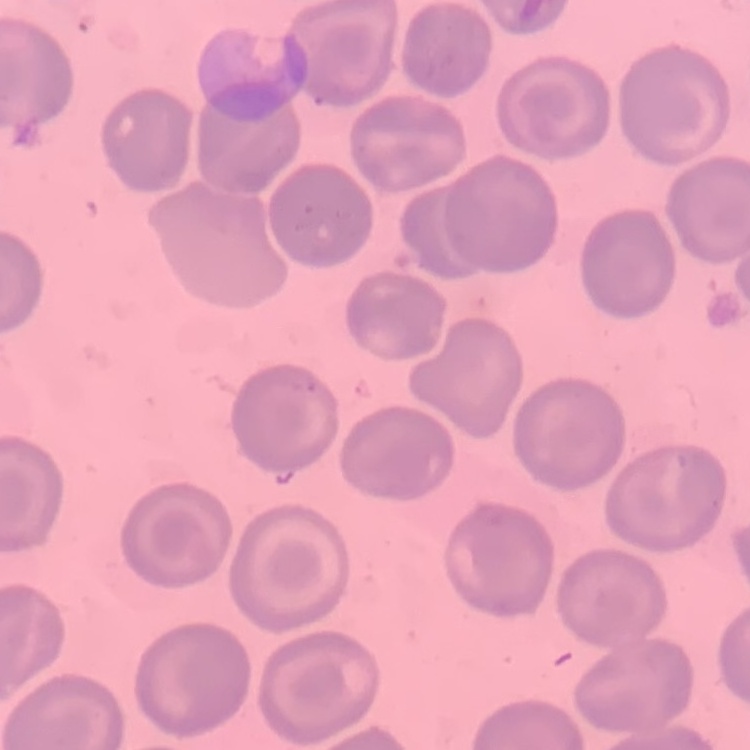
{
  "red_blood_cell_morphology": "no rouleaux formation",
  "preparation": "thin peripheral smear",
  "stain": "Field's or Giemsa",
  "image_type": "square crop of a larger photomicrograph"
}